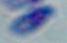
{
  "identification": "Toxoplasma gondii",
  "magnification": "1000x",
  "modality": "photomicrograph"
}